Locate every Plasmodium parasite.
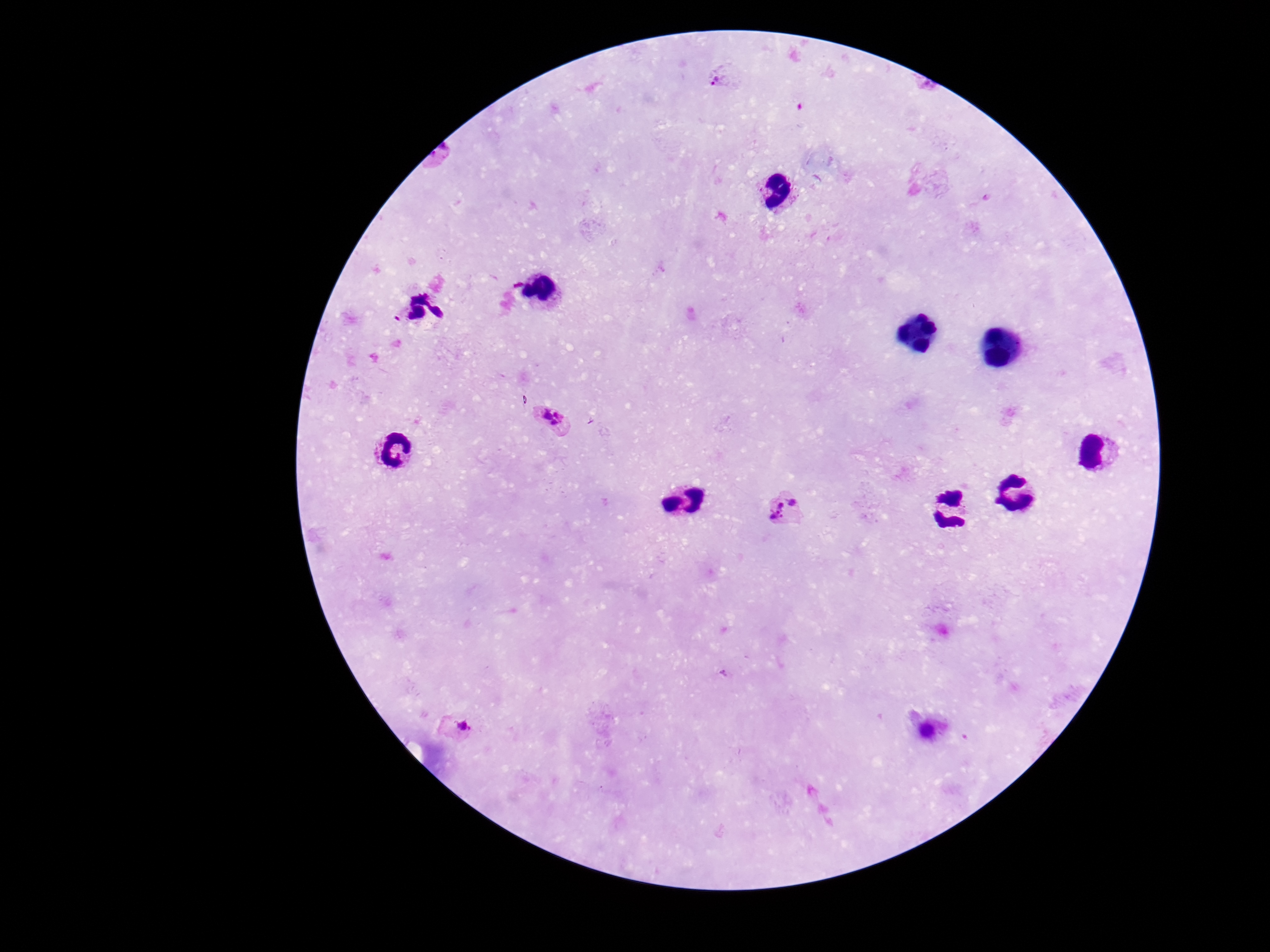

Approximate centers as [x, y] in pixels.
Plasmodium parasites: [725, 77], [551, 421], [788, 511], [456, 728].

Summary:
  - Preparation: thick blood film
  - Field of view: one from this slide
  - Image size: 1270×952 pixels
  - Capture: smartphone camera through the microscope eyepiece
  - Patient malaria status: positive
  - Magnification: 100x
  - Stain: Giemsa